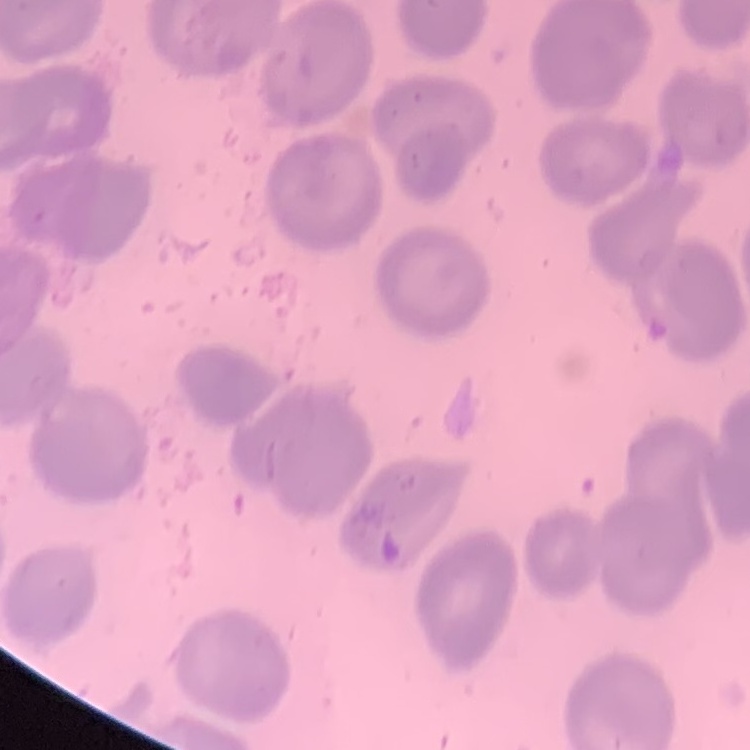

The erythrocytes show no rouleaux formation. One tile cut from a larger photomicrograph. Field's or Giemsa stain. Thin blood film.